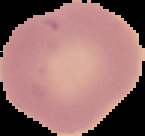
Summary:
  - Preparation: thin blood film
  - Malaria status: uninfected
  - Image type: segmented cell region on a black background
  - Image size: 145×136 pixels